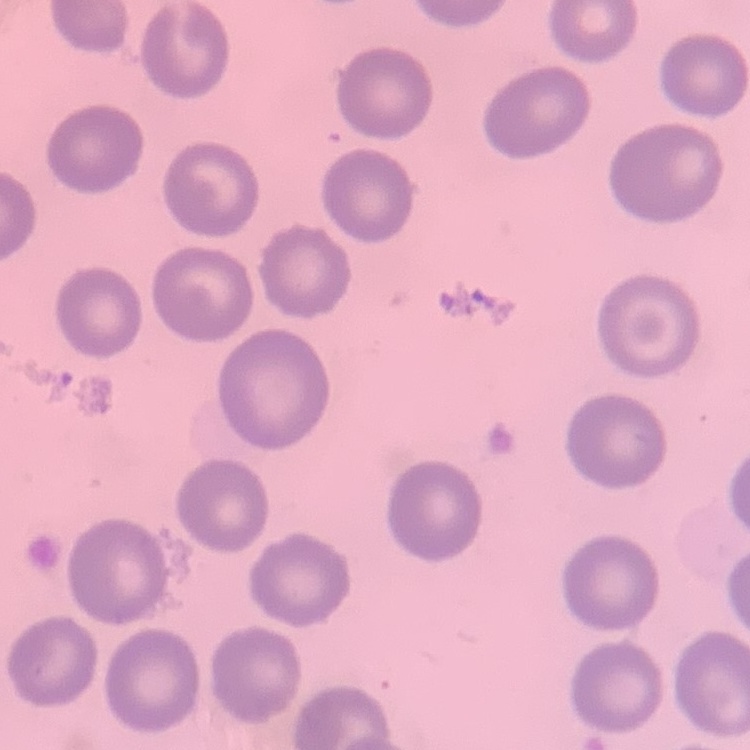

red blood cell morphology = no rouleaux formation
preparation = thin blood smear
image type = one tile cut from a larger photomicrograph
stain = Field's or Giemsa